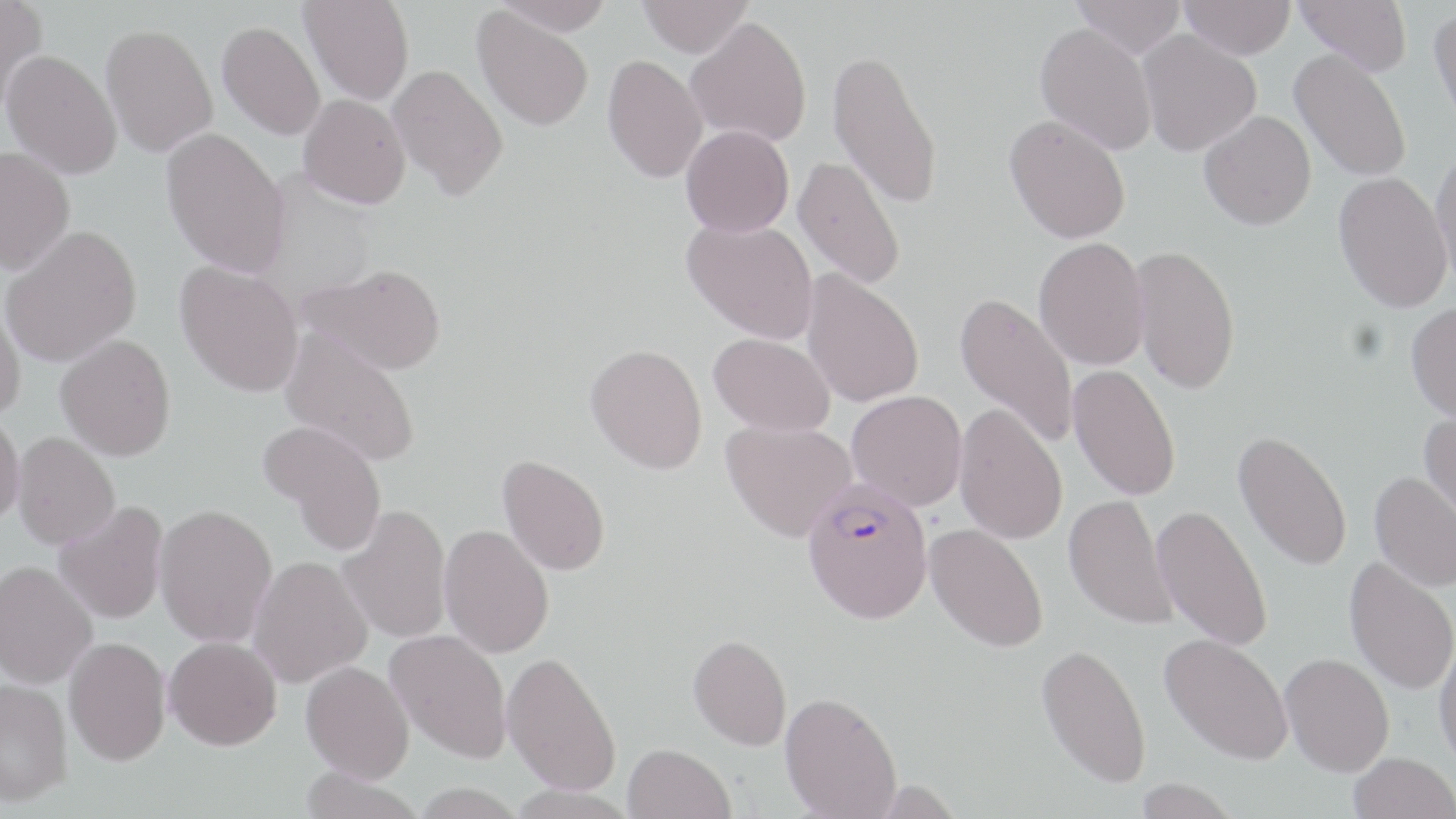 Approximate bounding boxes as named x1/y1/x2/y2 corners in pixels. Uninfected red blood cell locations: (x1=0, y1=0, x2=48, y2=118), (x1=299, y1=0, x2=414, y2=105), (x1=491, y1=0, x2=616, y2=35), (x1=638, y1=0, x2=753, y2=57), (x1=1071, y1=0, x2=1186, y2=59), (x1=1179, y1=0, x2=1296, y2=59), (x1=1295, y1=0, x2=1412, y2=75), (x1=472, y1=7, x2=594, y2=131), (x1=1429, y1=7, x2=1456, y2=132), (x1=686, y1=17, x2=812, y2=146), (x1=1034, y1=22, x2=1158, y2=155), (x1=216, y1=23, x2=325, y2=142), (x1=101, y1=28, x2=218, y2=160), (x1=1137, y1=30, x2=1262, y2=156), (x1=827, y1=46, x2=944, y2=212), (x1=1289, y1=48, x2=1412, y2=183), (x1=1, y1=53, x2=122, y2=181), (x1=601, y1=55, x2=707, y2=184), (x1=387, y1=64, x2=508, y2=200), (x1=298, y1=94, x2=411, y2=209), (x1=1198, y1=109, x2=1316, y2=230), (x1=1005, y1=114, x2=1131, y2=244), (x1=681, y1=125, x2=794, y2=237), (x1=160, y1=128, x2=290, y2=279), (x1=1430, y1=146, x2=1456, y2=294), (x1=0, y1=147, x2=76, y2=278), (x1=792, y1=154, x2=906, y2=290), (x1=1333, y1=172, x2=1452, y2=314), (x1=683, y1=218, x2=819, y2=344), (x1=1, y1=227, x2=142, y2=368), (x1=1033, y1=237, x2=1150, y2=370), (x1=1130, y1=243, x2=1240, y2=394), (x1=174, y1=260, x2=305, y2=398), (x1=300, y1=262, x2=447, y2=374), (x1=801, y1=269, x2=924, y2=408), (x1=954, y1=291, x2=1079, y2=449), (x1=0, y1=297, x2=26, y2=423), (x1=1406, y1=302, x2=1456, y2=424), (x1=279, y1=328, x2=421, y2=467), (x1=709, y1=333, x2=835, y2=436), (x1=55, y1=334, x2=176, y2=462), (x1=586, y1=344, x2=708, y2=474), (x1=1068, y1=365, x2=1181, y2=501), (x1=847, y1=390, x2=967, y2=510), (x1=954, y1=403, x2=1068, y2=544), (x1=1418, y1=411, x2=1456, y2=534), (x1=0, y1=413, x2=25, y2=528), (x1=259, y1=419, x2=388, y2=555), (x1=720, y1=419, x2=857, y2=542), (x1=1233, y1=430, x2=1353, y2=571), (x1=11, y1=431, x2=119, y2=549), (x1=497, y1=454, x2=611, y2=576), (x1=1369, y1=470, x2=1456, y2=591), (x1=1064, y1=494, x2=1177, y2=630), (x1=53, y1=501, x2=169, y2=625), (x1=153, y1=503, x2=279, y2=647), (x1=337, y1=504, x2=452, y2=644), (x1=1152, y1=504, x2=1273, y2=652), (x1=925, y1=523, x2=1049, y2=652), (x1=439, y1=524, x2=555, y2=658), (x1=247, y1=556, x2=372, y2=688), (x1=1344, y1=557, x2=1456, y2=696), (x1=0, y1=560, x2=98, y2=689), (x1=385, y1=629, x2=512, y2=762), (x1=688, y1=634, x2=791, y2=750), (x1=1160, y1=634, x2=1294, y2=765), (x1=1434, y1=634, x2=1456, y2=774), (x1=164, y1=635, x2=282, y2=750), (x1=64, y1=636, x2=171, y2=765), (x1=1036, y1=642, x2=1152, y2=789), (x1=502, y1=650, x2=622, y2=795), (x1=1280, y1=653, x2=1394, y2=776), (x1=300, y1=660, x2=414, y2=783), (x1=0, y1=678, x2=73, y2=806), (x1=780, y1=691, x2=902, y2=818), (x1=623, y1=743, x2=736, y2=819), (x1=1348, y1=752, x2=1455, y2=819), (x1=299, y1=767, x2=424, y2=819), (x1=1132, y1=778, x2=1240, y2=819), (x1=409, y1=784, x2=527, y2=819). Plasmodium falciparum-infected red blood cell locations: (x1=801, y1=481, x2=934, y2=624). Slide-level diagnosis: Plasmodium falciparum. One field of a larger specimen. Thin blood smear. May-Grünwald-Giemsa stain. Optical microscopy. Image is 1456×819 pixels. Captured at 1000x magnification.